Name the parasite shown.
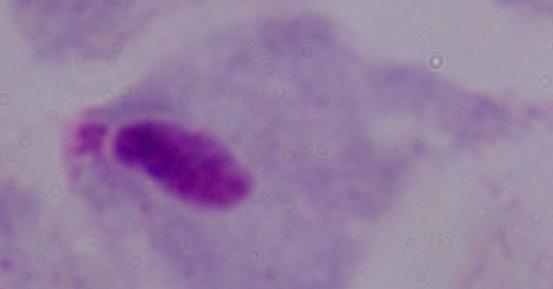
A trichomonad.

Summary:
  - Modality: photomicrograph
  - Magnification: 1000x